Rate the background quality.
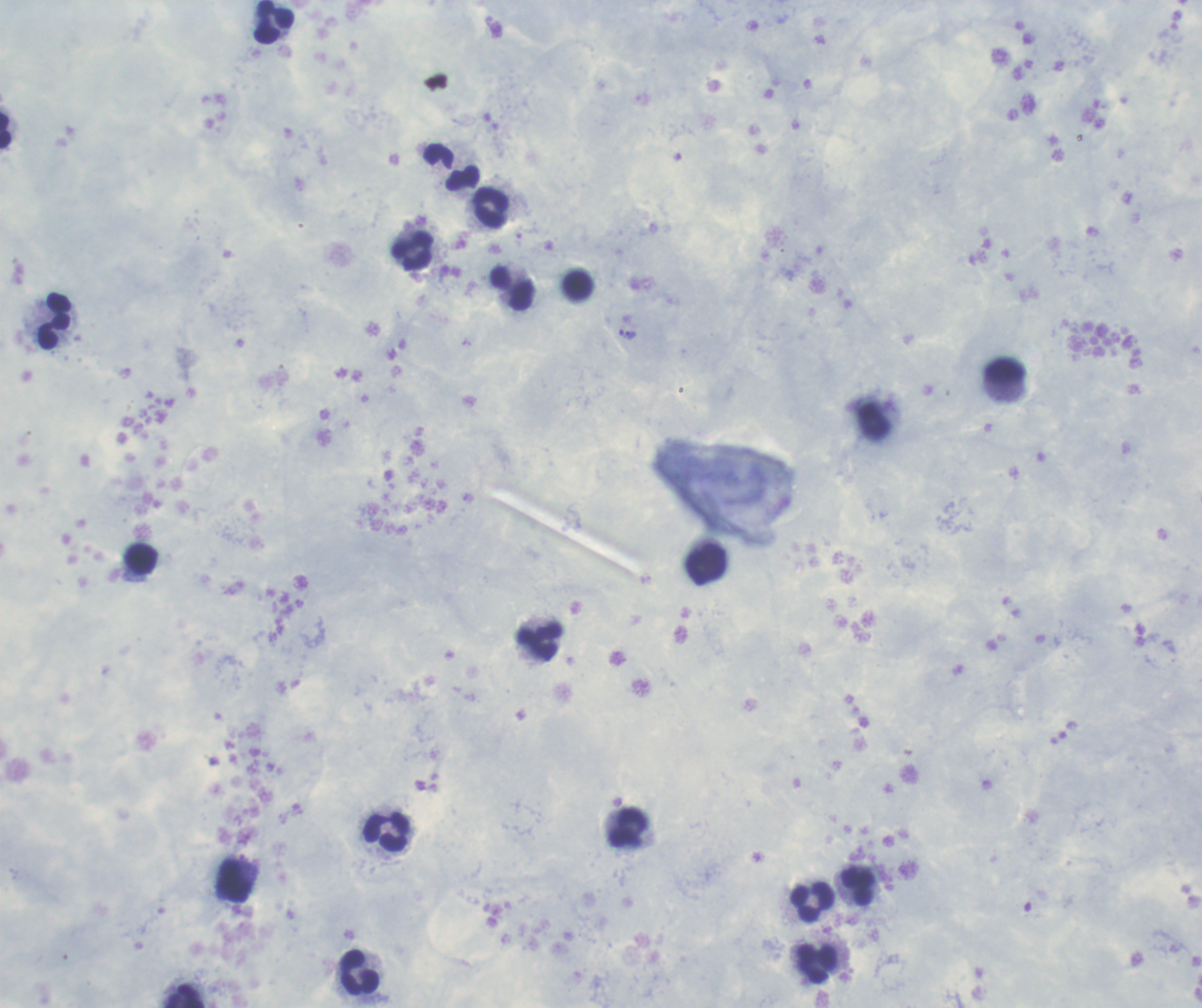

Satisfactory.

Approximate centers as {x, y} in pixels.
Summary:
  - Leukocyte locations: {274, 23}, {6, 133}, {451, 169}, {491, 208}, {413, 251}, {514, 288}, {54, 321}, {1007, 371}, {141, 559}, {707, 565}, {540, 643}, {628, 826}, {387, 832}, {235, 883}, {859, 886}, {814, 902}, {817, 963}, {358, 972}, {185, 996}
  - Trophozoite locations: {631, 336}
  - Result: Plasmodium parasites identified
  - Field of view: one from this slide
  - Coloration quality: good
  - Preparation: thick smear of blood
  - Magnification: 100x
  - Stain: Romanowsky
  - Context: previously used in an actual diagnosis
  - Image size: 1202×1008 pixels